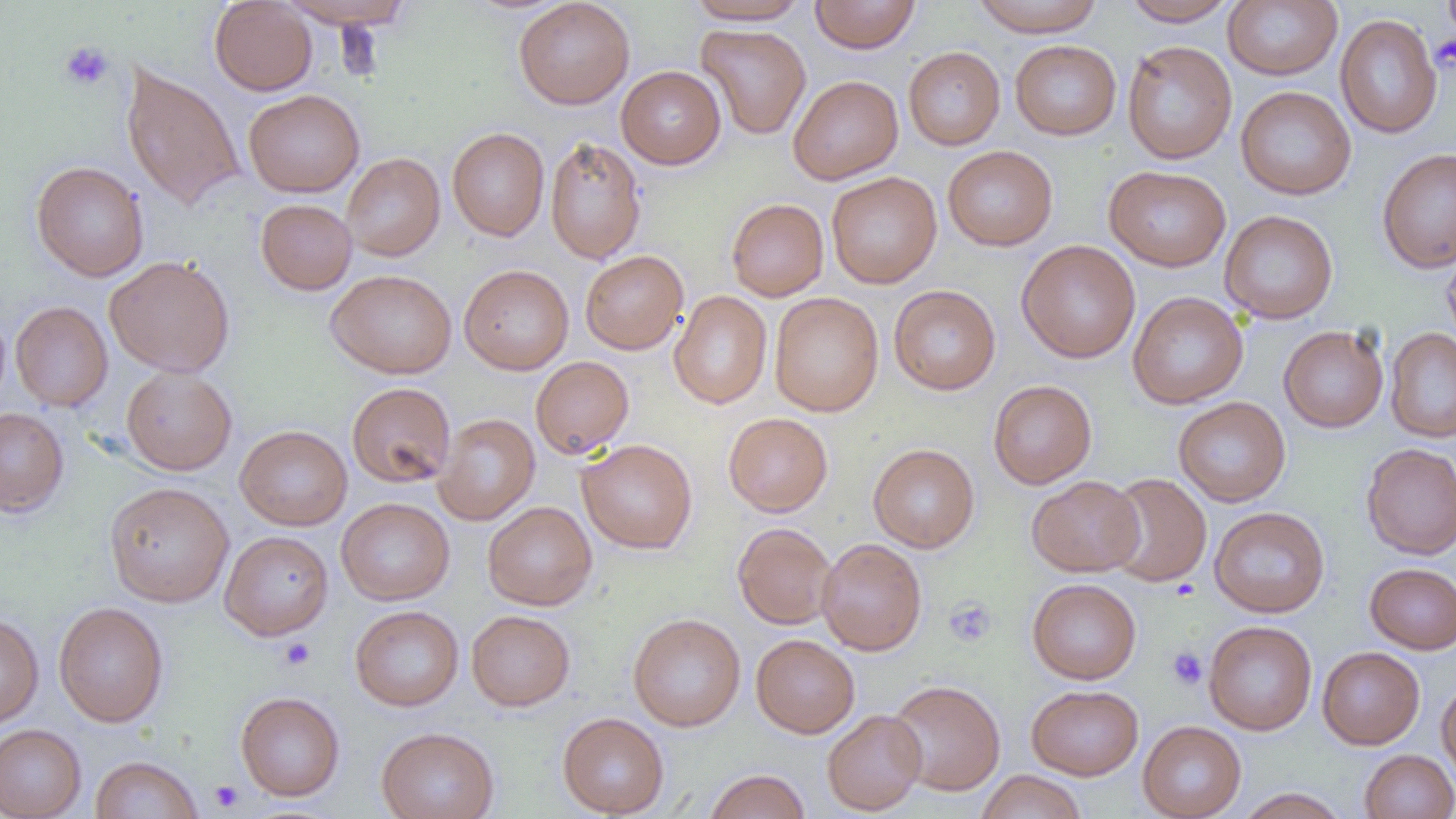

slide-level diagnosis = negative for blood parasites
preparation = thin blood film
uninfected red blood cell locations = approximate bounding boxes as named x1/y1/x2/y2 corners in pixels: (x1=209, y1=0, x2=317, y2=96), (x1=276, y1=0, x2=416, y2=29), (x1=514, y1=0, x2=635, y2=109), (x1=685, y1=0, x2=812, y2=25), (x1=809, y1=0, x2=921, y2=54), (x1=971, y1=0, x2=1104, y2=36), (x1=1121, y1=0, x2=1240, y2=26), (x1=1223, y1=1, x2=1343, y2=80), (x1=1335, y1=14, x2=1443, y2=138), (x1=696, y1=24, x2=811, y2=139), (x1=1010, y1=40, x2=1121, y2=140), (x1=1122, y1=40, x2=1237, y2=164), (x1=903, y1=46, x2=1005, y2=150), (x1=121, y1=62, x2=246, y2=212), (x1=616, y1=66, x2=726, y2=169), (x1=788, y1=75, x2=903, y2=184), (x1=1235, y1=86, x2=1356, y2=200), (x1=243, y1=89, x2=365, y2=197), (x1=447, y1=127, x2=549, y2=241), (x1=545, y1=136, x2=646, y2=264), (x1=942, y1=145, x2=1058, y2=251), (x1=1377, y1=148, x2=1456, y2=273), (x1=341, y1=153, x2=445, y2=261), (x1=31, y1=161, x2=149, y2=282), (x1=1104, y1=165, x2=1231, y2=271), (x1=826, y1=171, x2=942, y2=288), (x1=726, y1=198, x2=829, y2=301), (x1=256, y1=199, x2=357, y2=294), (x1=1219, y1=210, x2=1338, y2=324), (x1=1016, y1=240, x2=1141, y2=363), (x1=1441, y1=241, x2=1456, y2=351), (x1=580, y1=250, x2=688, y2=354), (x1=105, y1=255, x2=236, y2=376), (x1=459, y1=264, x2=574, y2=375), (x1=326, y1=269, x2=457, y2=379), (x1=888, y1=284, x2=1001, y2=395), (x1=669, y1=290, x2=772, y2=409), (x1=769, y1=292, x2=884, y2=417), (x1=1127, y1=292, x2=1248, y2=409), (x1=10, y1=301, x2=112, y2=411), (x1=1278, y1=326, x2=1388, y2=432), (x1=1385, y1=328, x2=1456, y2=443), (x1=531, y1=356, x2=634, y2=459), (x1=121, y1=366, x2=237, y2=475), (x1=988, y1=380, x2=1097, y2=489), (x1=347, y1=382, x2=456, y2=488), (x1=1173, y1=396, x2=1291, y2=507), (x1=0, y1=407, x2=69, y2=517), (x1=723, y1=412, x2=833, y2=517), (x1=433, y1=413, x2=540, y2=525), (x1=235, y1=424, x2=352, y2=530), (x1=577, y1=438, x2=697, y2=554), (x1=868, y1=443, x2=980, y2=553), (x1=1361, y1=443, x2=1456, y2=559), (x1=1103, y1=473, x2=1212, y2=587), (x1=1027, y1=475, x2=1143, y2=577), (x1=104, y1=481, x2=234, y2=608), (x1=336, y1=497, x2=455, y2=605), (x1=482, y1=501, x2=597, y2=610), (x1=1209, y1=506, x2=1330, y2=618), (x1=732, y1=522, x2=837, y2=629), (x1=220, y1=530, x2=334, y2=640), (x1=817, y1=538, x2=927, y2=656), (x1=1365, y1=562, x2=1456, y2=654), (x1=1027, y1=578, x2=1142, y2=684), (x1=53, y1=601, x2=169, y2=727), (x1=350, y1=605, x2=464, y2=711), (x1=466, y1=609, x2=575, y2=711), (x1=0, y1=613, x2=44, y2=728), (x1=628, y1=613, x2=746, y2=732), (x1=1204, y1=620, x2=1317, y2=735), (x1=751, y1=634, x2=860, y2=738), (x1=1317, y1=646, x2=1425, y2=749), (x1=1436, y1=678, x2=1456, y2=785), (x1=887, y1=680, x2=1006, y2=795), (x1=1027, y1=684, x2=1143, y2=780), (x1=235, y1=691, x2=345, y2=801), (x1=822, y1=709, x2=927, y2=815), (x1=557, y1=712, x2=669, y2=817), (x1=1137, y1=720, x2=1247, y2=818), (x1=0, y1=724, x2=86, y2=819), (x1=376, y1=726, x2=499, y2=819), (x1=1359, y1=749, x2=1456, y2=819), (x1=90, y1=755, x2=203, y2=818), (x1=703, y1=769, x2=811, y2=819), (x1=976, y1=770, x2=1087, y2=819), (x1=1235, y1=788, x2=1350, y2=819)
field of view = single
image size = 1456×819 pixels
platelet locations = approximate bounding boxes as named x1/y1/x2/y2 corners in pixels: (x1=1441, y1=0, x2=1456, y2=41), (x1=1432, y1=32, x2=1456, y2=74), (x1=59, y1=40, x2=115, y2=91), (x1=945, y1=597, x2=997, y2=646), (x1=278, y1=637, x2=316, y2=671), (x1=1167, y1=646, x2=1208, y2=690), (x1=209, y1=780, x2=244, y2=812)
modality = optical microscopy
magnification = 1000x